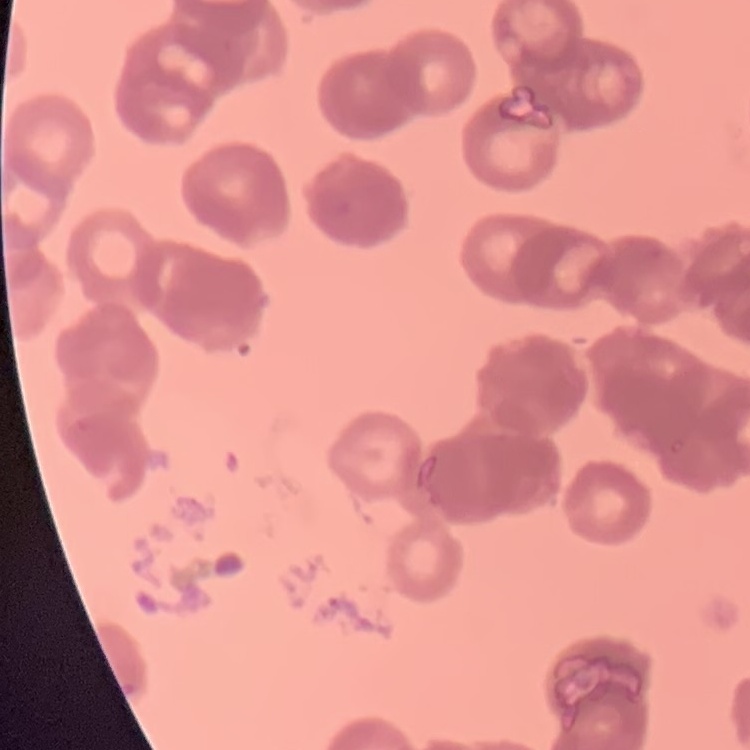
Summary:
  - Erythrocyte morphology: rouleaux formation
  - Preparation: thin peripheral smear
  - Image type: one tile cut from a larger photomicrograph
  - Stain: Field's or Giemsa